Identify the blood parasite species.
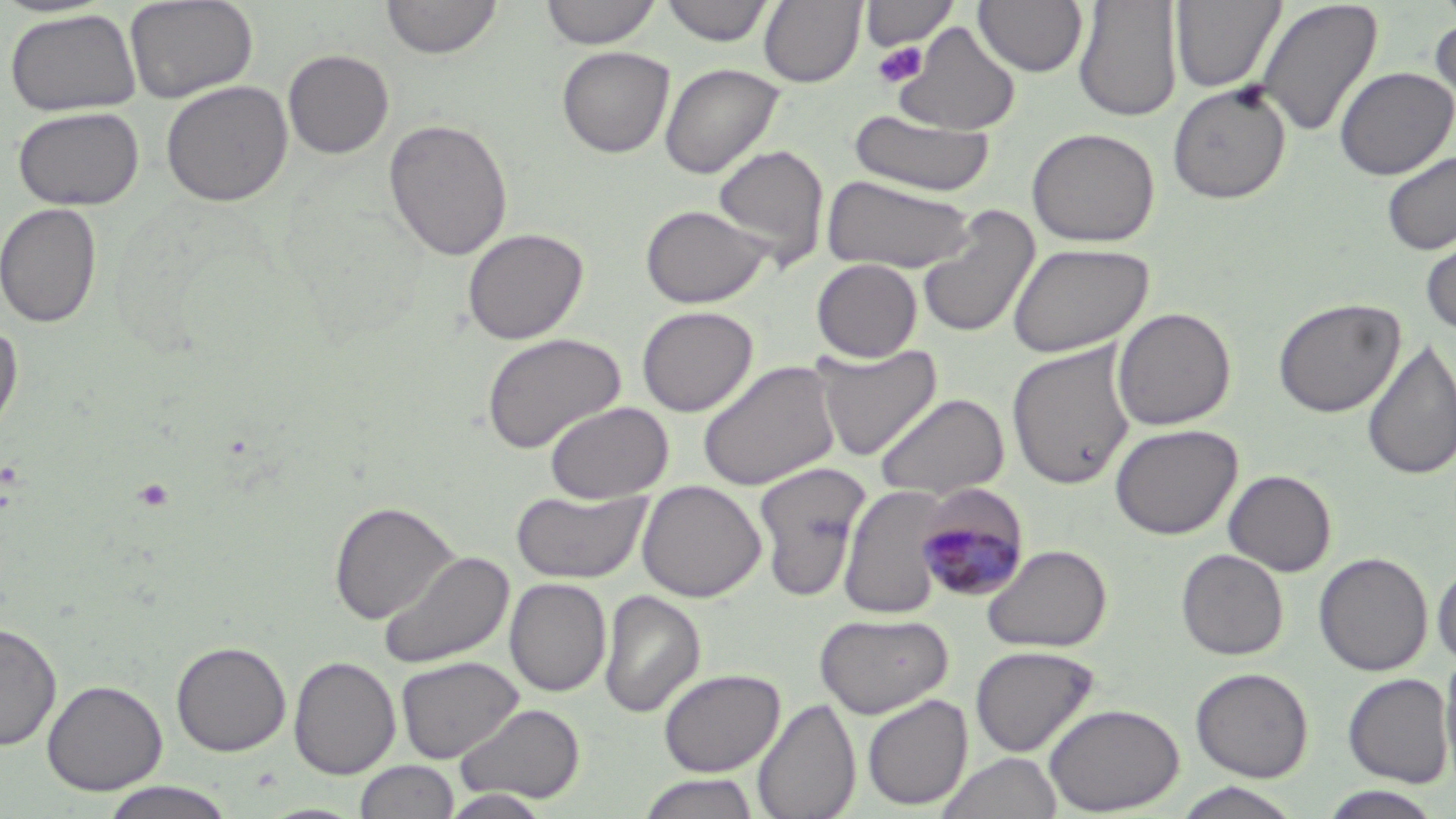

Plasmodium malariae.

magnification: 1000x
field_of_view: one of a larger specimen
image_size: 1456×819 pixels
preparation: thin blood film
plasmodium_malariae_infected_red_blood_cell_locations: 'approximate bounding boxes as named x1/y1/x2/y2 corners in pixels: (x1=914, y1=486, x2=1029, y2=603)'
uninfected_red_blood_cell_locations: 'approximate bounding boxes as named x1/y1/x2/y2 corners in pixels: (x1=124, y1=0, x2=258, y2=103), (x1=381, y1=0, x2=502, y2=60), (x1=540, y1=0, x2=662, y2=50), (x1=660, y1=0, x2=774, y2=46), (x1=759, y1=0, x2=865, y2=87), (x1=974, y1=0, x2=1088, y2=77), (x1=1073, y1=0, x2=1182, y2=122), (x1=1170, y1=0, x2=1285, y2=93), (x1=861, y1=1, x2=959, y2=52), (x1=1256, y1=1, x2=1384, y2=138), (x1=4, y1=9, x2=141, y2=116), (x1=1429, y1=15, x2=1456, y2=125), (x1=893, y1=22, x2=1020, y2=136), (x1=557, y1=46, x2=675, y2=158), (x1=283, y1=49, x2=394, y2=160), (x1=659, y1=63, x2=784, y2=178), (x1=1334, y1=66, x2=1454, y2=180), (x1=160, y1=80, x2=293, y2=206), (x1=1168, y1=82, x2=1291, y2=204), (x1=12, y1=106, x2=144, y2=211), (x1=848, y1=108, x2=995, y2=197), (x1=384, y1=118, x2=512, y2=262), (x1=1026, y1=127, x2=1160, y2=247), (x1=712, y1=144, x2=829, y2=270), (x1=1380, y1=150, x2=1456, y2=256), (x1=822, y1=175, x2=976, y2=273), (x1=0, y1=201, x2=102, y2=328), (x1=639, y1=204, x2=771, y2=308), (x1=915, y1=205, x2=1040, y2=339), (x1=1420, y1=225, x2=1456, y2=338), (x1=462, y1=228, x2=588, y2=344), (x1=1007, y1=242, x2=1153, y2=358), (x1=812, y1=259, x2=922, y2=362), (x1=1273, y1=297, x2=1404, y2=417), (x1=636, y1=306, x2=758, y2=416), (x1=1113, y1=307, x2=1235, y2=430), (x1=0, y1=320, x2=24, y2=438), (x1=481, y1=332, x2=625, y2=453), (x1=1362, y1=338, x2=1456, y2=481), (x1=812, y1=344, x2=941, y2=460), (x1=1006, y1=344, x2=1135, y2=490), (x1=697, y1=359, x2=840, y2=491), (x1=873, y1=392, x2=1010, y2=501), (x1=544, y1=401, x2=673, y2=503), (x1=1110, y1=423, x2=1242, y2=540), (x1=753, y1=462, x2=871, y2=601), (x1=1223, y1=469, x2=1336, y2=576), (x1=636, y1=480, x2=766, y2=602), (x1=838, y1=483, x2=952, y2=619), (x1=511, y1=489, x2=649, y2=584), (x1=329, y1=501, x2=457, y2=624), (x1=983, y1=544, x2=1112, y2=653), (x1=378, y1=549, x2=514, y2=671), (x1=1176, y1=549, x2=1289, y2=660), (x1=1314, y1=552, x2=1433, y2=676), (x1=1433, y1=561, x2=1456, y2=667), (x1=505, y1=578, x2=610, y2=697), (x1=598, y1=590, x2=705, y2=718), (x1=815, y1=612, x2=953, y2=718), (x1=0, y1=620, x2=62, y2=751), (x1=171, y1=641, x2=291, y2=756), (x1=970, y1=645, x2=1099, y2=758), (x1=1439, y1=650, x2=1456, y2=784), (x1=395, y1=655, x2=523, y2=763), (x1=289, y1=656, x2=400, y2=779), (x1=1190, y1=667, x2=1313, y2=781), (x1=658, y1=668, x2=785, y2=776), (x1=1342, y1=672, x2=1454, y2=787), (x1=42, y1=679, x2=166, y2=795), (x1=861, y1=694, x2=972, y2=810), (x1=753, y1=698, x2=861, y2=819), (x1=456, y1=703, x2=585, y2=804), (x1=1044, y1=703, x2=1184, y2=815), (x1=937, y1=751, x2=1062, y2=819), (x1=354, y1=760, x2=459, y2=818), (x1=635, y1=773, x2=762, y2=818), (x1=97, y1=781, x2=240, y2=818), (x1=1171, y1=782, x2=1305, y2=819), (x1=1317, y1=787, x2=1445, y2=819), (x1=440, y1=789, x2=553, y2=818)'
stain: May-Grünwald-Giemsa
modality: light microscopy
platelet_locations: 'approximate bounding boxes as named x1/y1/x2/y2 corners in pixels: (x1=872, y1=41, x2=928, y2=89), (x1=132, y1=477, x2=176, y2=513)'